Locate and identify every blood parasite.
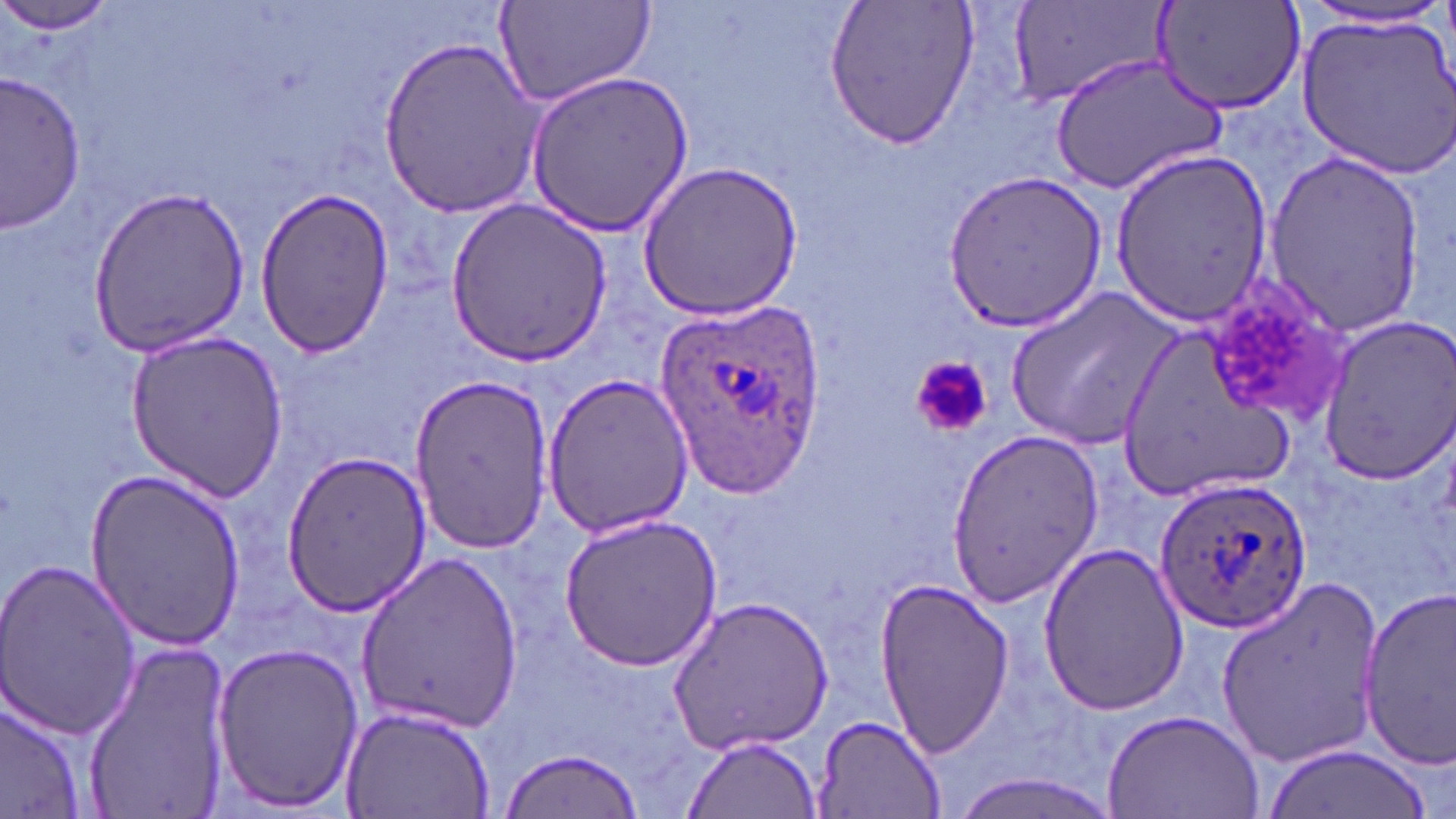

Approximate bounding boxes as (x1, y1, x2, y2) in pixels.
Plasmodium ovale-infected red blood cells: (653, 298, 823, 501), (1153, 475, 1310, 631).
No Plasmodium falciparum, Plasmodium malariae, Plasmodium vivax, Babesia divergens, or Trypanosoma brucei observed.

Uninfected red blood cell locations: (1, 0, 117, 42), (493, 0, 656, 111), (823, 0, 979, 150), (1011, 0, 1171, 111), (1154, 0, 1306, 117), (1289, 3, 1452, 34), (1297, 12, 1456, 178), (378, 36, 546, 218), (1051, 52, 1227, 197), (521, 69, 697, 237), (1, 72, 85, 232), (1109, 147, 1271, 323), (1261, 150, 1427, 339), (640, 161, 806, 319), (943, 168, 1108, 332), (87, 184, 251, 357), (253, 189, 397, 356), (446, 198, 614, 367), (1200, 276, 1356, 428), (1008, 286, 1186, 453), (1317, 316, 1456, 481), (1115, 325, 1298, 507), (125, 327, 290, 500), (539, 372, 694, 536), (408, 375, 556, 555), (939, 430, 1106, 602), (281, 448, 433, 620), (82, 467, 246, 652), (558, 511, 724, 671), (1036, 542, 1188, 717), (355, 551, 524, 738), (1, 555, 141, 741), (1217, 577, 1389, 768), (872, 579, 1016, 759), (1357, 586, 1456, 770), (667, 597, 835, 755), (80, 639, 234, 818), (209, 639, 365, 814), (0, 691, 86, 817), (340, 702, 497, 818), (1103, 707, 1265, 819), (812, 713, 946, 818), (682, 732, 822, 818), (1264, 742, 1432, 819), (498, 747, 645, 819), (938, 771, 1127, 819). Platelet locations: (908, 354, 992, 439). Slide-level diagnosis: Plasmodium ovale. Optical microscopy. Image is 1456×819 pixels. 1000x magnification. Single field of view. May-Grünwald-Giemsa stain. Thin blood smear.